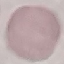
Summary:
  - Malaria status: uninfected
  - Image type: automatically extracted cell patch, resized to 64 × 64 pixels
  - Capture: smartphone through the microscope eyepiece
  - Preparation: thin smear
  - Stain: Giemsa